Describe the morphology of the erythrocytes.
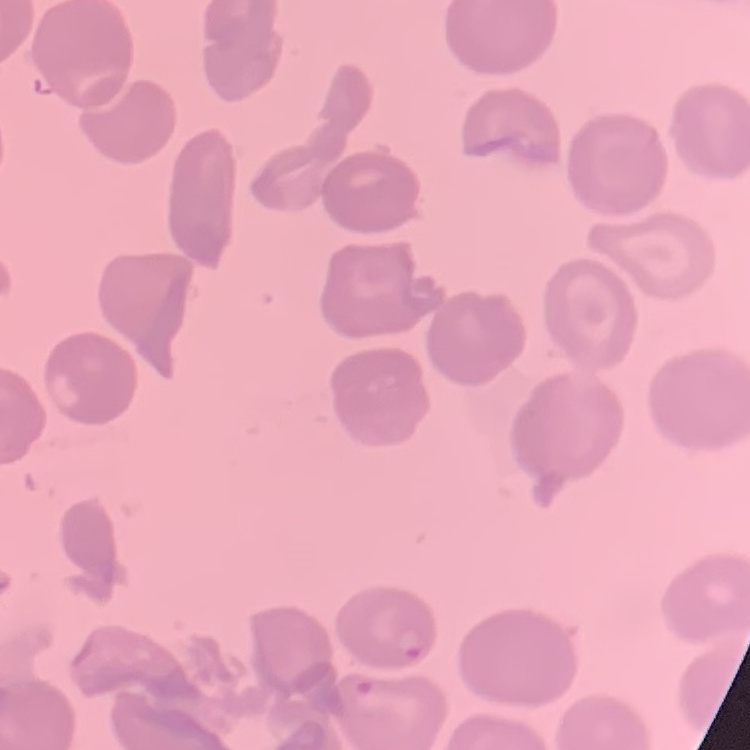

They show no rouleaux formation.

Summary:
  - Image type: square crop of a larger photomicrograph
  - Preparation: thin peripheral smear
  - Stain: Field's or Giemsa